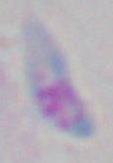

identification: Toxoplasma gondii
magnification: 1000x
modality: photomicrograph